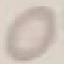

Malaria status: uninfected. Thin blood film. Acquired by smartphone through the microscope eyepiece. Giemsa-stained preparation. Automatically extracted cell patch, resized to 64 × 64 pixels.